Locate every Plasmodium vivax-infected red blood cell.
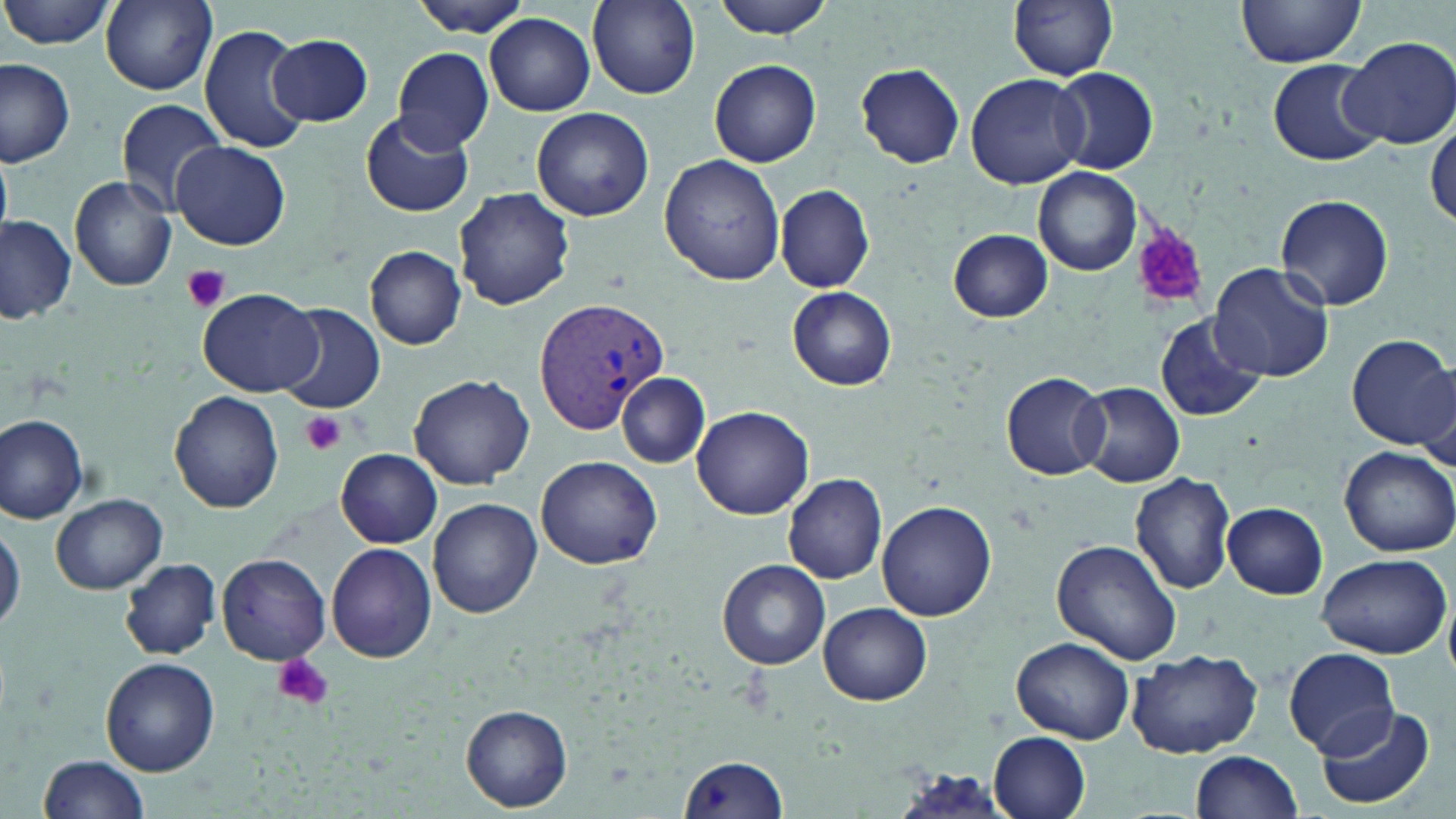

Approximate bounding boxes as [x1, y1, x2, y2] in pixels.
Plasmodium vivax-infected red blood cells: [532, 292, 671, 435].

slide_level_diagnosis: Plasmodium vivax
magnification: 1000x
preparation: thin blood smear
stain: May-Grünwald-Giemsa
uninfected_red_blood_cell_locations: 'approximate bounding boxes as [x1, y1, x2, y2] in pixels: [2, 0, 117, 50], [100, 0, 218, 93], [409, 0, 535, 35], [712, 0, 837, 39], [1008, 0, 1120, 81], [1235, 1, 1367, 67], [589, 2, 701, 99], [485, 13, 596, 115], [198, 23, 310, 153], [267, 34, 373, 127], [1340, 36, 1456, 151], [392, 47, 496, 151], [0, 57, 77, 168], [709, 58, 822, 167], [1268, 59, 1385, 164], [856, 63, 965, 167], [1052, 67, 1158, 175], [966, 72, 1090, 188], [115, 98, 228, 213], [531, 107, 653, 220], [359, 108, 474, 218], [1427, 116, 1456, 229], [170, 140, 291, 250], [0, 154, 12, 237], [659, 154, 786, 286], [1033, 166, 1142, 276], [69, 176, 180, 291], [774, 184, 875, 293], [453, 188, 576, 312], [1276, 193, 1396, 311], [1, 217, 77, 326], [948, 228, 1053, 321], [365, 246, 466, 349], [1208, 263, 1335, 384], [786, 285, 897, 390], [197, 289, 325, 398], [275, 304, 387, 414], [1154, 313, 1267, 423], [1348, 334, 1456, 449], [1002, 370, 1111, 479], [409, 373, 535, 488], [616, 373, 710, 467], [1076, 381, 1185, 488], [169, 392, 283, 513], [691, 403, 815, 520], [0, 412, 92, 524], [1340, 446, 1455, 556], [336, 449, 442, 547], [535, 455, 661, 570], [1130, 472, 1236, 594], [784, 473, 888, 584], [49, 491, 166, 594], [429, 498, 541, 618], [877, 500, 997, 621], [1223, 503, 1328, 599], [0, 521, 24, 636], [1053, 540, 1182, 666], [325, 542, 438, 662], [1315, 551, 1452, 658], [217, 553, 330, 665], [718, 559, 831, 670], [120, 560, 221, 659], [819, 603, 932, 706], [1012, 638, 1135, 743], [1127, 647, 1265, 758], [1283, 647, 1396, 756], [100, 656, 219, 775], [1313, 702, 1439, 813], [460, 705, 572, 812], [989, 732, 1090, 817], [1191, 749, 1300, 817], [40, 754, 151, 818], [677, 755, 789, 818]'
image_size: 1456×819 pixels
modality: optical microscopy
field_of_view: single
platelet_locations: 'approximate bounding boxes as [x1, y1, x2, y2] in pixels: [1134, 228, 1210, 310], [181, 263, 232, 313], [300, 410, 346, 455], [272, 652, 334, 711]'